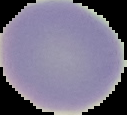
From a thin blood film. Result: negative for malaria parasites. Image is 127×115 pixels. Segmented cell region on a black background.